Assess the morphology of the red blood cells.
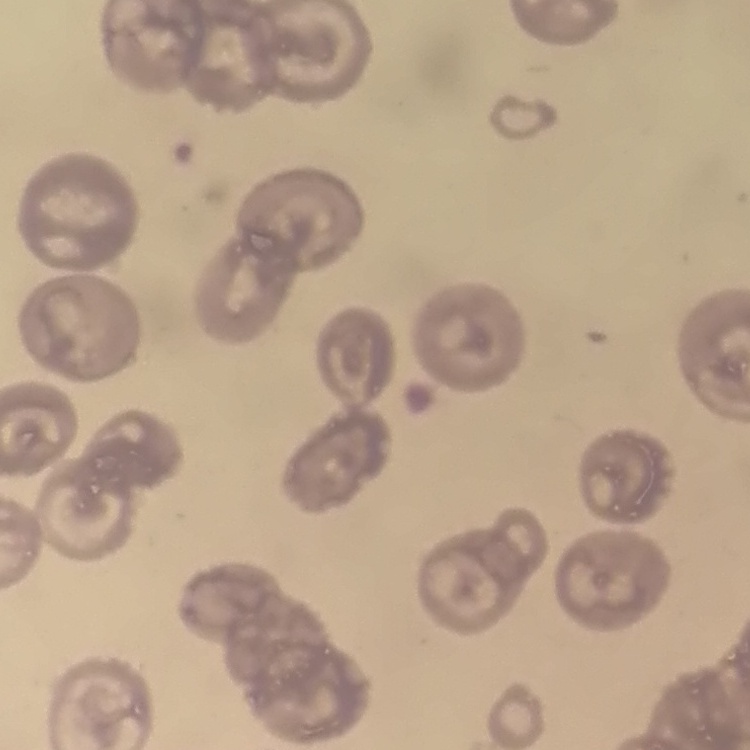

They show no rouleaux formation.

One tile cut from a larger photomicrograph. Stained with either Field's or Giemsa. Thin peripheral smear.